Identify the parasite.
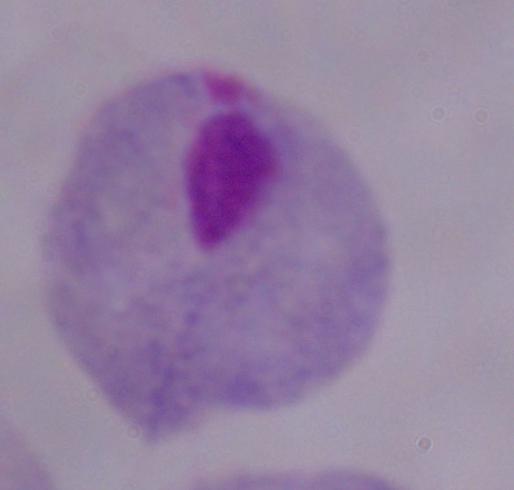
A trichomonad.

Summary:
  - Modality: micrograph
  - Magnification: 1000x